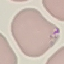
Summary:
  - Malaria status: parasitized
  - Image type: automatically extracted cell patch, resized to 64 × 64 pixels
  - Preparation: thin blood smear
  - Capture: smartphone through the microscope eyepiece
  - Stain: Giemsa